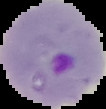

{
  "image_type": "segmented cell region with the area outside set to black",
  "preparation": "thin blood smear",
  "result": "malaria parasites identified",
  "image_size": "106×109 pixels"
}